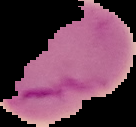
Summary:
  - Image type: cell region segmented out of the field of view; surrounding area masked to black
  - Image size: 136×127 pixels
  - Preparation: thin blood smear
  - Result: Plasmodium parasites detected